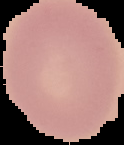

image size = 124×145 pixels
image type = segmented cell region with the area outside set to black
malaria status = uninfected
preparation = thin blood film